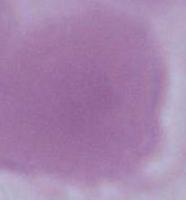
Micrograph. A red blood cell is seen. 1000x magnification.